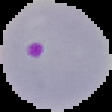
From a thin blood smear. Image is 112×112 pixels. The area outside the segmented cell region is set to black. Malaria status: parasitized.